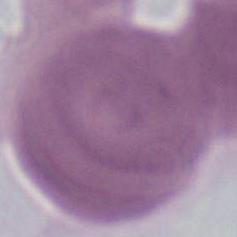 An erythrocyte is seen. Photomicrograph. Captured at 1000x magnification.